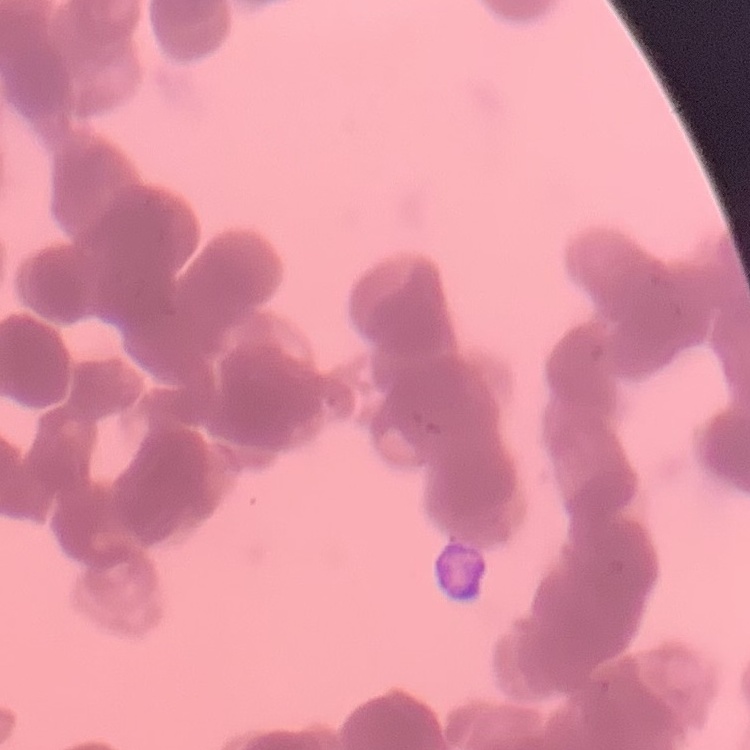 The erythrocytes show rouleaux formation. Thin blood film. Square crop of a larger photomicrograph. Field's or Giemsa stain.